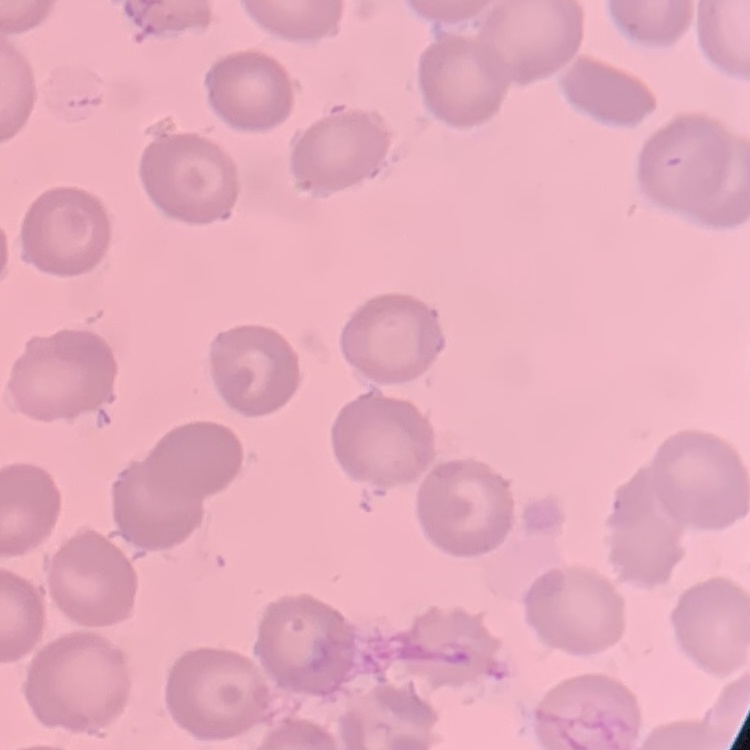

Summary:
  - Erythrocyte morphology: no rouleaux formation
  - Image type: square crop of a larger photomicrograph
  - Preparation: thin peripheral smear
  - Stain: Field's or Giemsa